Identify the parasite.
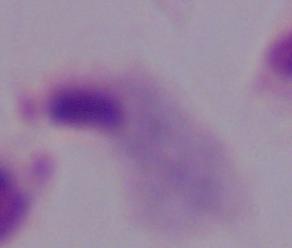

A trichomonad.

modality = photomicrograph
magnification = 1000x